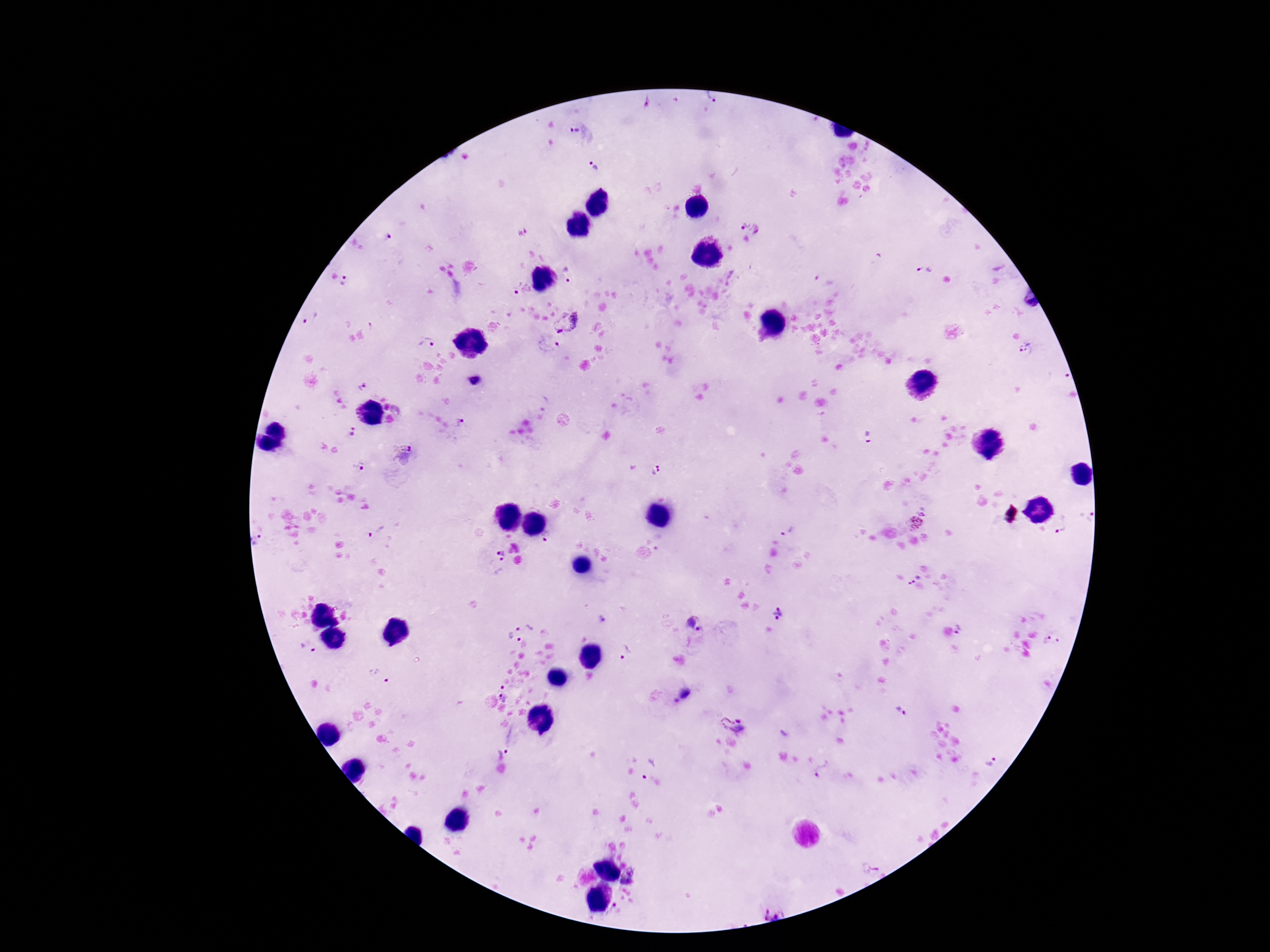

{
  "preparation": "thick blood film",
  "patient_malaria_status": "positive",
  "capture": "smartphone camera through the microscope eyepiece",
  "stain": "Giemsa",
  "plasmodium_parasite_locations": "approximate object centers, in pixels from the top-left corner: (x=713, y=97), (x=573, y=131), (x=594, y=167), (x=742, y=225), (x=758, y=229), (x=388, y=238), (x=925, y=271), (x=570, y=275), (x=344, y=280), (x=520, y=290), (x=311, y=317), (x=570, y=325), (x=428, y=344), (x=546, y=346), (x=1027, y=350), (x=475, y=380), (x=362, y=386), (x=460, y=422), (x=352, y=432), (x=868, y=436), (x=405, y=455), (x=358, y=466), (x=655, y=469), (x=1086, y=515), (x=1065, y=523), (x=914, y=524), (x=787, y=529), (x=376, y=530), (x=547, y=537), (x=258, y=543), (x=502, y=555), (x=913, y=577), (x=779, y=614), (x=603, y=618), (x=696, y=623), (x=524, y=624), (x=963, y=631), (x=1053, y=637), (x=511, y=641), (x=308, y=648), (x=626, y=651), (x=379, y=676), (x=503, y=687), (x=504, y=697), (x=682, y=698), (x=901, y=710), (x=734, y=723), (x=510, y=739), (x=993, y=763), (x=648, y=769), (x=823, y=772), (x=872, y=871), (x=632, y=879), (x=614, y=910), (x=774, y=910)",
  "field_of_view": "one from this slide",
  "image_size": "1270×952 pixels",
  "magnification": "100x"
}